Evaluate for Plasmodium parasites.
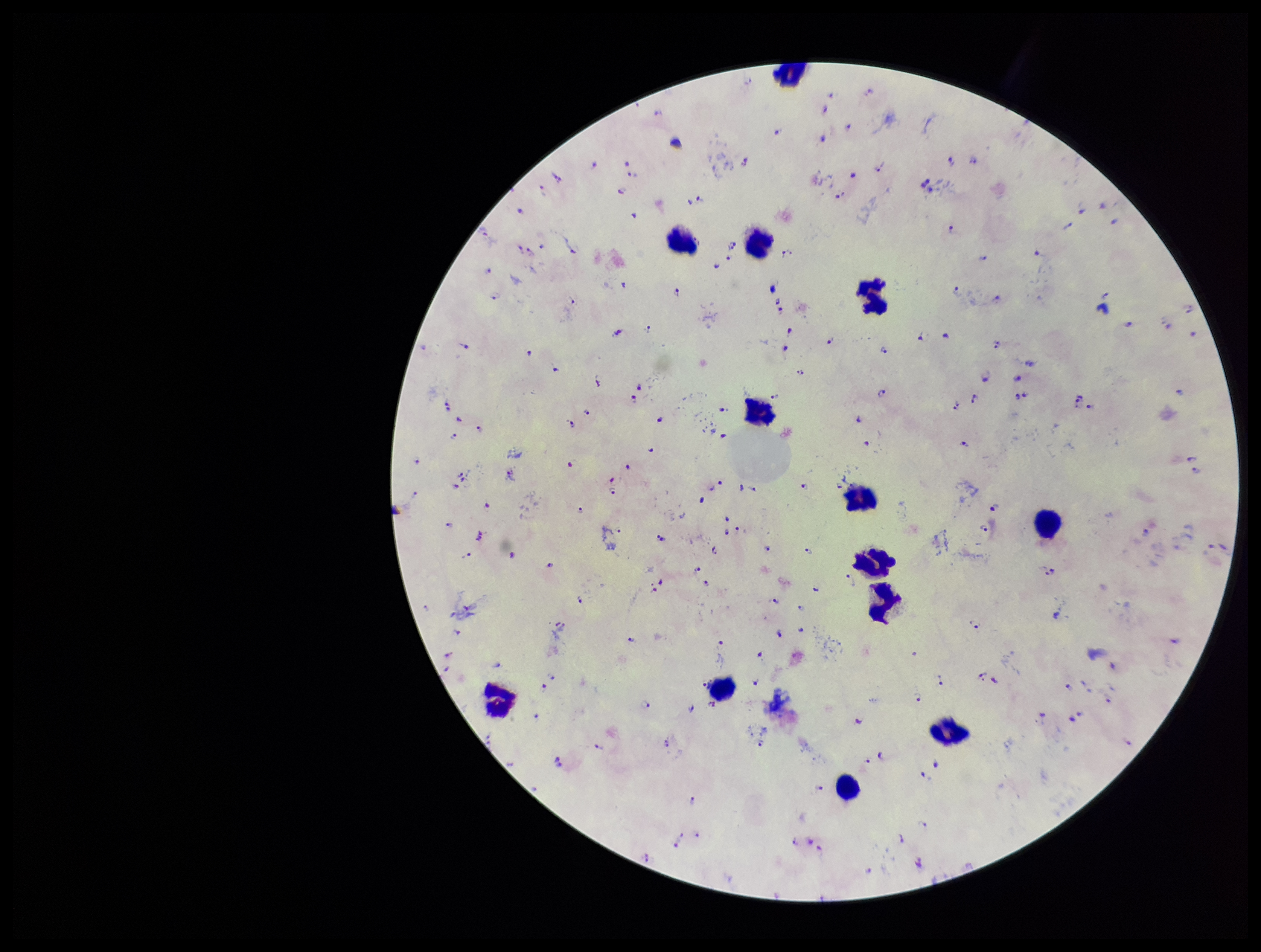

Identified.

Summary:
  - Species reported for this patient: Plasmodium falciparum
  - Field of view: one from this slide
  - Image size: 1261×952 pixels
  - Capture: smartphone photograph through the microscope eyepiece
  - Preparation: thick
  - Patient malaria status: infected
  - Parasite count: 150
  - Stain: Giemsa
  - Leukocyte count: 13